State which parasite is depicted.
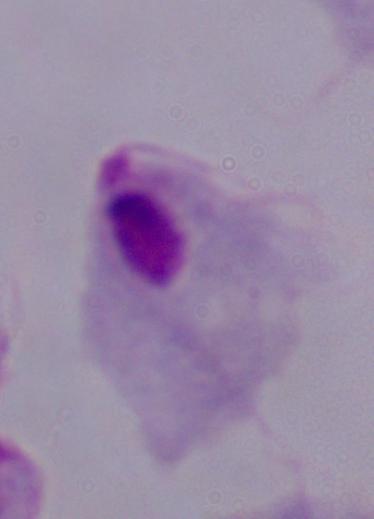
A trichomonad.

Photomicrograph. Captured at 1000x magnification.